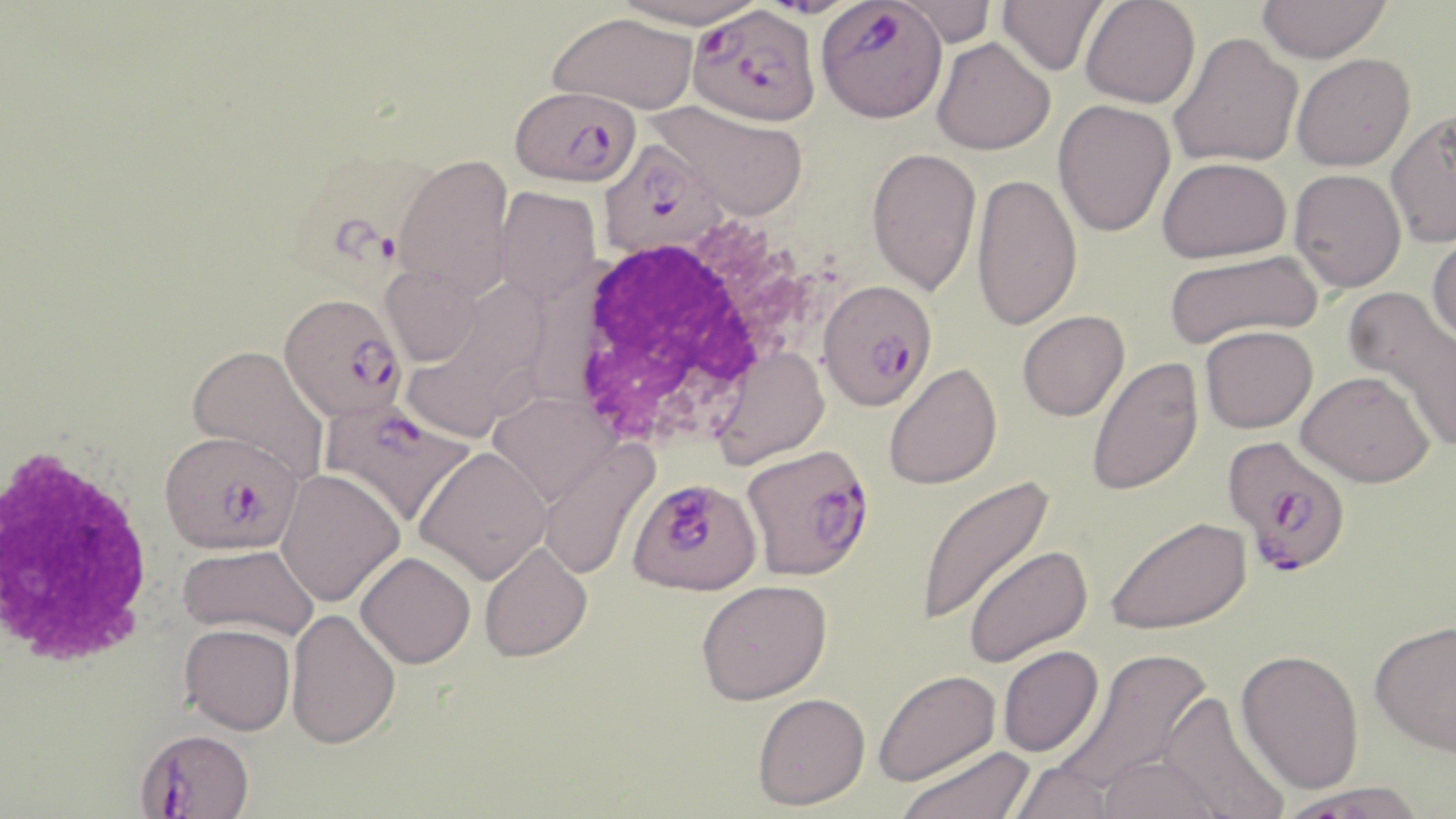
Summary:
  - Coordinate format: approximate bounding boxes as (x1, y1, x2, y2) in pixels
  - Plasmodium falciparum-infected red blood cell locations: (815, 1, 948, 123), (686, 4, 820, 126), (510, 85, 641, 187), (599, 140, 730, 261), (294, 153, 441, 296), (817, 278, 938, 410), (279, 292, 406, 422), (319, 399, 476, 527), (160, 429, 302, 555), (1223, 437, 1353, 577), (741, 443, 875, 580), (628, 477, 762, 596), (135, 728, 254, 818)
  - White blood cell locations: (558, 224, 811, 453), (0, 441, 159, 671)
  - Uninfected red blood cell locations: (611, 0, 765, 29), (997, 0, 1108, 76), (1080, 0, 1201, 109), (1256, 0, 1392, 64), (887, 1, 1000, 46), (548, 12, 698, 115), (1168, 32, 1304, 168), (931, 36, 1055, 155), (1291, 53, 1415, 171), (650, 99, 810, 221), (1052, 99, 1176, 237), (1385, 109, 1456, 248), (866, 146, 982, 296), (393, 154, 515, 298), (1157, 156, 1292, 263), (1289, 169, 1407, 293), (971, 172, 1082, 331), (493, 186, 601, 303), (1427, 228, 1456, 347), (1162, 249, 1323, 349), (379, 264, 482, 366), (1343, 286, 1455, 436), (1017, 310, 1129, 421), (1200, 324, 1318, 433), (186, 343, 330, 485), (713, 347, 830, 468), (1085, 355, 1204, 496), (883, 362, 1002, 490), (1296, 370, 1435, 487), (489, 392, 617, 505), (538, 440, 659, 580), (414, 446, 551, 583), (275, 469, 404, 607), (913, 474, 1056, 627), (1105, 515, 1253, 635), (479, 540, 593, 662), (177, 544, 318, 641), (963, 544, 1093, 668), (355, 551, 476, 668), (696, 578, 832, 704), (285, 608, 401, 749), (1369, 618, 1456, 756), (179, 622, 296, 735), (997, 645, 1104, 758), (1053, 647, 1213, 798), (1235, 648, 1364, 794), (873, 669, 1001, 786), (1158, 690, 1290, 819), (752, 692, 870, 810), (897, 744, 1035, 819), (1098, 754, 1226, 819), (1005, 761, 1116, 819), (1275, 780, 1428, 819)
  - Slide-level diagnosis: Plasmodium falciparum
  - Modality: optical microscopy
  - Image size: 1456×819 pixels
  - Field of view: single
  - Stain: May-Grünwald-Giemsa
  - Preparation: thin blood smear
  - Magnification: 1000x